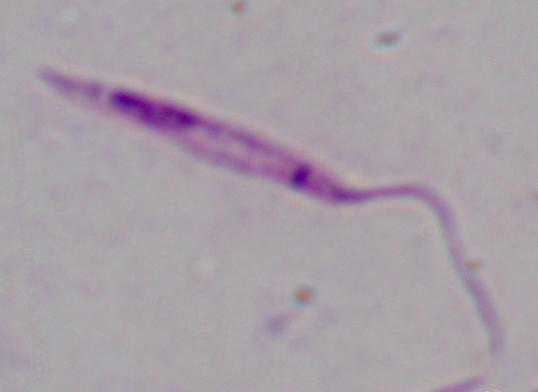
Summary:
  - Identification: Leishmania
  - Magnification: 1000x
  - Modality: micrograph